Report the malaria status of this cell.
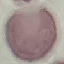

Uninfected.

Photographed with a smartphone camera at the microscope eyepiece. Giemsa-stained preparation. Thin blood film. Automatically extracted cell patch, resized to 64 × 64 pixels.